Mark where platelets are.
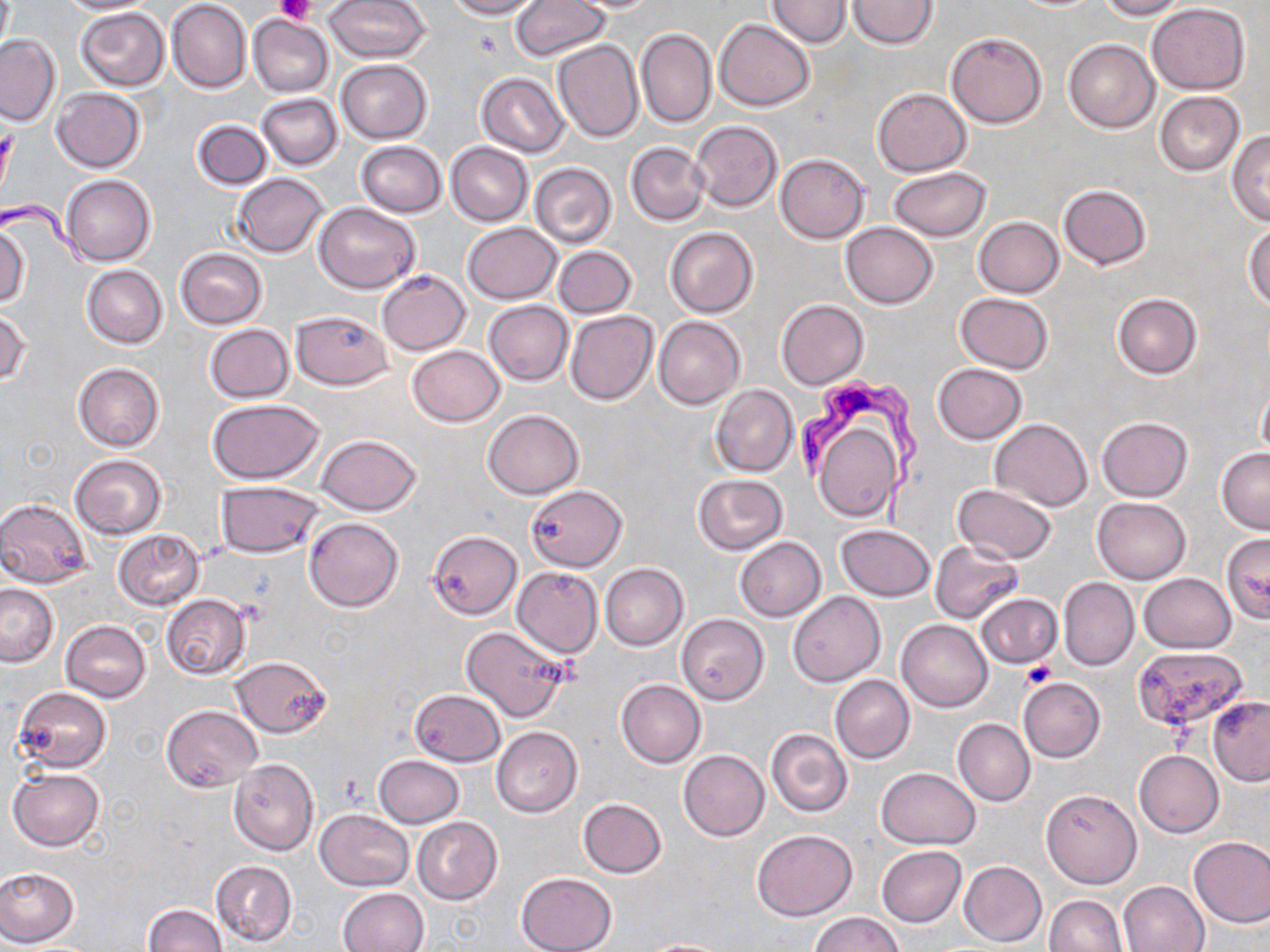

Approximate bounding boxes as (x1,y1)-(x2,y2) corner pairs in pixels.
Platelets: (276,0)-(314,24), (472,29)-(503,59), (1020,661)-(1056,690).

Uninfected red blood cell locations: (55,0)-(157,15), (324,0)-(430,62), (443,0)-(541,20), (767,0)-(852,47), (848,0)-(940,48), (1096,0)-(1187,20), (167,1)-(251,93), (512,1)-(610,61), (566,1)-(665,13), (1148,3)-(1251,94), (75,7)-(169,90), (248,14)-(334,97), (715,18)-(815,111), (637,28)-(716,128), (945,31)-(1047,127), (0,35)-(61,125), (552,39)-(644,143), (1063,39)-(1158,132), (337,59)-(432,143), (476,73)-(569,157), (872,87)-(972,176), (52,89)-(146,173), (1155,90)-(1245,176), (256,94)-(343,170), (192,119)-(272,189), (690,120)-(782,212), (1227,132)-(1270,225), (355,141)-(446,217), (446,142)-(534,226), (626,142)-(709,226), (775,152)-(870,244), (530,163)-(616,247), (888,167)-(991,242), (232,173)-(329,258), (60,176)-(155,265), (1058,184)-(1152,270), (314,203)-(421,293), (974,217)-(1065,298), (1243,221)-(1270,310), (462,222)-(562,304), (841,223)-(938,309), (0,224)-(29,308), (665,227)-(759,318), (552,246)-(637,318), (175,248)-(267,329), (82,266)-(167,348), (377,270)-(471,355), (956,293)-(1052,375), (1112,294)-(1201,379), (484,300)-(573,386), (776,300)-(868,388), (0,308)-(30,387), (290,309)-(393,389), (565,310)-(658,405), (655,316)-(745,408), (205,324)-(294,402), (674,344)-(764,444), (405,345)-(505,427), (72,363)-(164,452), (931,364)-(1028,444), (1256,384)-(1270,463), (710,386)-(798,477), (208,399)-(323,483), (483,409)-(583,500), (809,416)-(903,523), (1097,416)-(1193,500), (990,419)-(1093,511), (317,434)-(420,515), (1216,447)-(1270,533), (70,454)-(167,539), (694,474)-(787,554), (217,482)-(323,559), (952,484)-(1056,563), (525,487)-(628,572), (0,498)-(92,588), (1092,498)-(1191,583), (305,518)-(404,612), (835,525)-(935,601), (114,530)-(204,609), (430,532)-(523,620), (1220,532)-(1270,622), (735,536)-(826,621), (929,540)-(1024,623), (600,563)-(689,651), (512,567)-(603,658), (1138,573)-(1235,652), (1058,576)-(1139,671), (0,583)-(57,667), (788,592)-(884,687), (161,594)-(251,678), (975,594)-(1062,669), (677,614)-(768,705), (897,619)-(992,712), (60,621)-(151,702), (460,625)-(569,722), (1136,644)-(1247,740), (229,655)-(330,737), (830,675)-(915,763), (1018,677)-(1105,762), (616,680)-(705,767), (12,688)-(111,770), (410,690)-(505,766), (1207,696)-(1270,785), (1175,699)-(1261,811), (161,704)-(262,791), (953,718)-(1035,806), (491,726)-(582,818), (766,728)-(853,818), (1135,749)-(1224,837), (679,750)-(770,841), (374,755)-(463,827), (229,758)-(318,856), (876,767)-(979,848), (9,768)-(104,851), (1042,790)-(1140,888), (578,798)-(668,878), (315,808)-(414,891), (413,816)-(502,905), (751,829)-(858,921), (1188,836)-(1270,928), (877,846)-(967,926), (210,859)-(297,947), (959,860)-(1047,946), (0,866)-(79,948), (515,872)-(617,952), (1117,881)-(1209,952), (338,889)-(427,951), (1043,894)-(1128,952), (142,904)-(227,952), (810,913)-(903,952), (640,938)-(737,951). Trypanosoma brucei locations: (797,372)-(928,526). Slide-level diagnosis: Trypanosoma brucei. Thin blood smear. Captured at 1000x magnification. May-Grünwald-Giemsa stain. Light microscopy. Image is 1270×952 pixels. Single field of view.